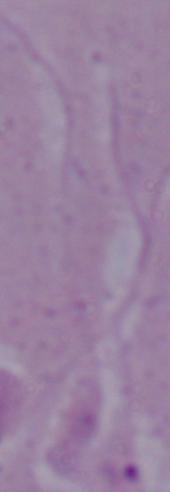
Micrograph. A Leishmania parasite is seen. 1000x magnification.